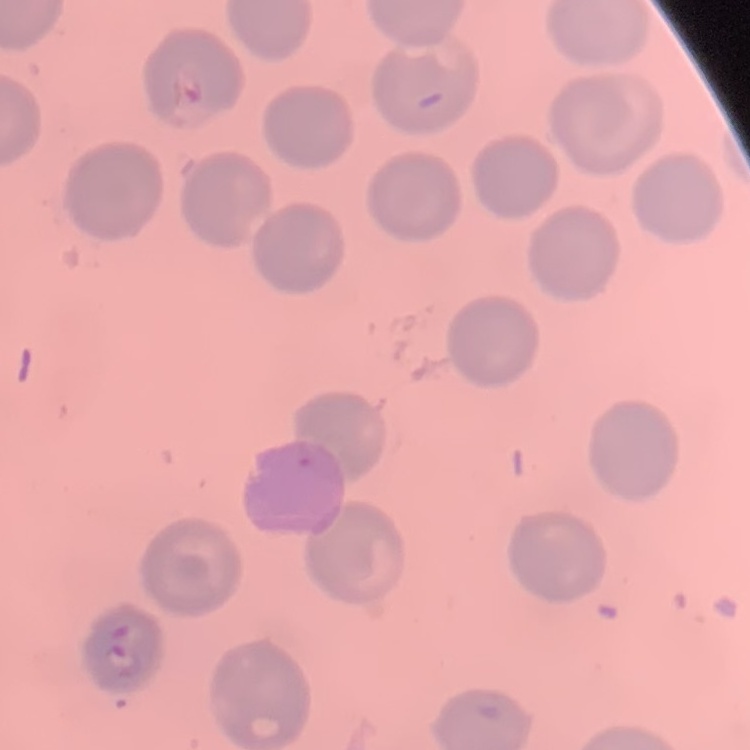

red blood cell morphology = no rouleaux formation
stain = Field's or Giemsa
image type = one tile cut from a larger photomicrograph
preparation = thin blood smear